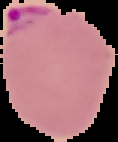

Summary:
  - Malaria status: parasitized
  - Image size: 118×142 pixels
  - Preparation: thin blood smear
  - Image type: segmented cell region on a black background